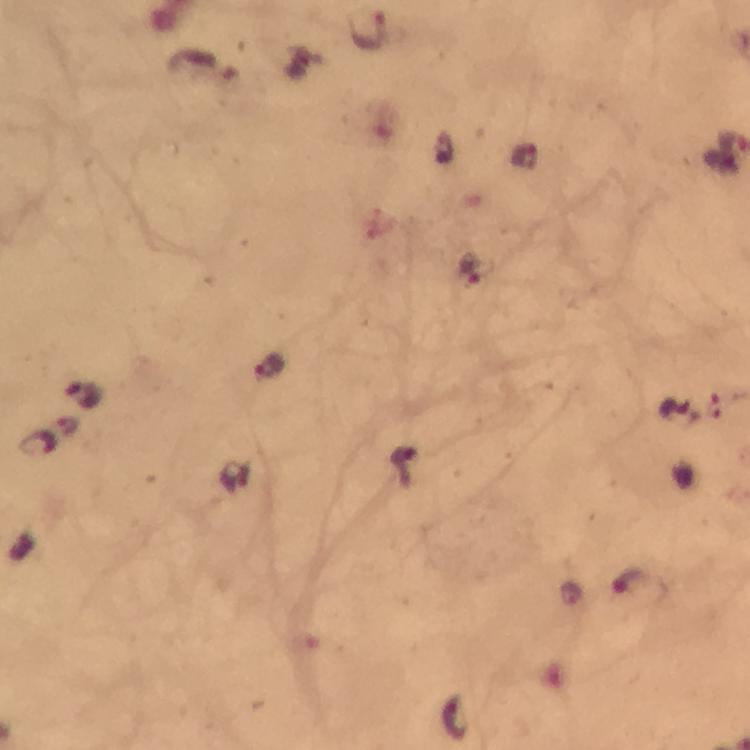

Plasmodium parasite locations = approximate object centers, in pixels from the top-left corner: (x=368, y=32), (x=525, y=157), (x=470, y=267), (x=269, y=366), (x=81, y=393), (x=679, y=413), (x=36, y=444), (x=234, y=476), (x=636, y=581)
capture = smartphone mounted on the microscope
context = from a malaria diagnostic workup
preparation = thick blood film
cropped from = a single field of view
immersion oil = applied
image size = 750×750 pixels
stain = Giemsa
magnification = 100x